Identify the parasite.
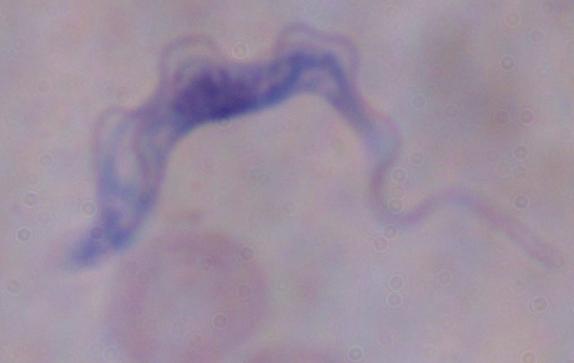

A trypanosome.

{
  "modality": "photomicrograph",
  "magnification": "1000x"
}